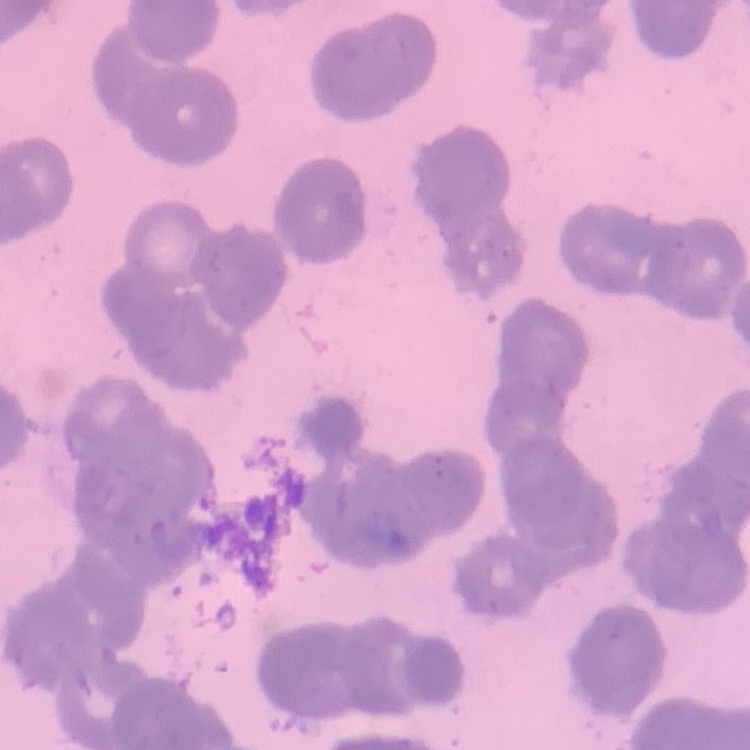

Summary:
  - Erythrocyte morphology: rouleaux formation
  - Image type: one tile cut from a larger photomicrograph
  - Preparation: thin blood smear
  - Stain: Field's or Giemsa